Outline each Trypanosoma brucei.
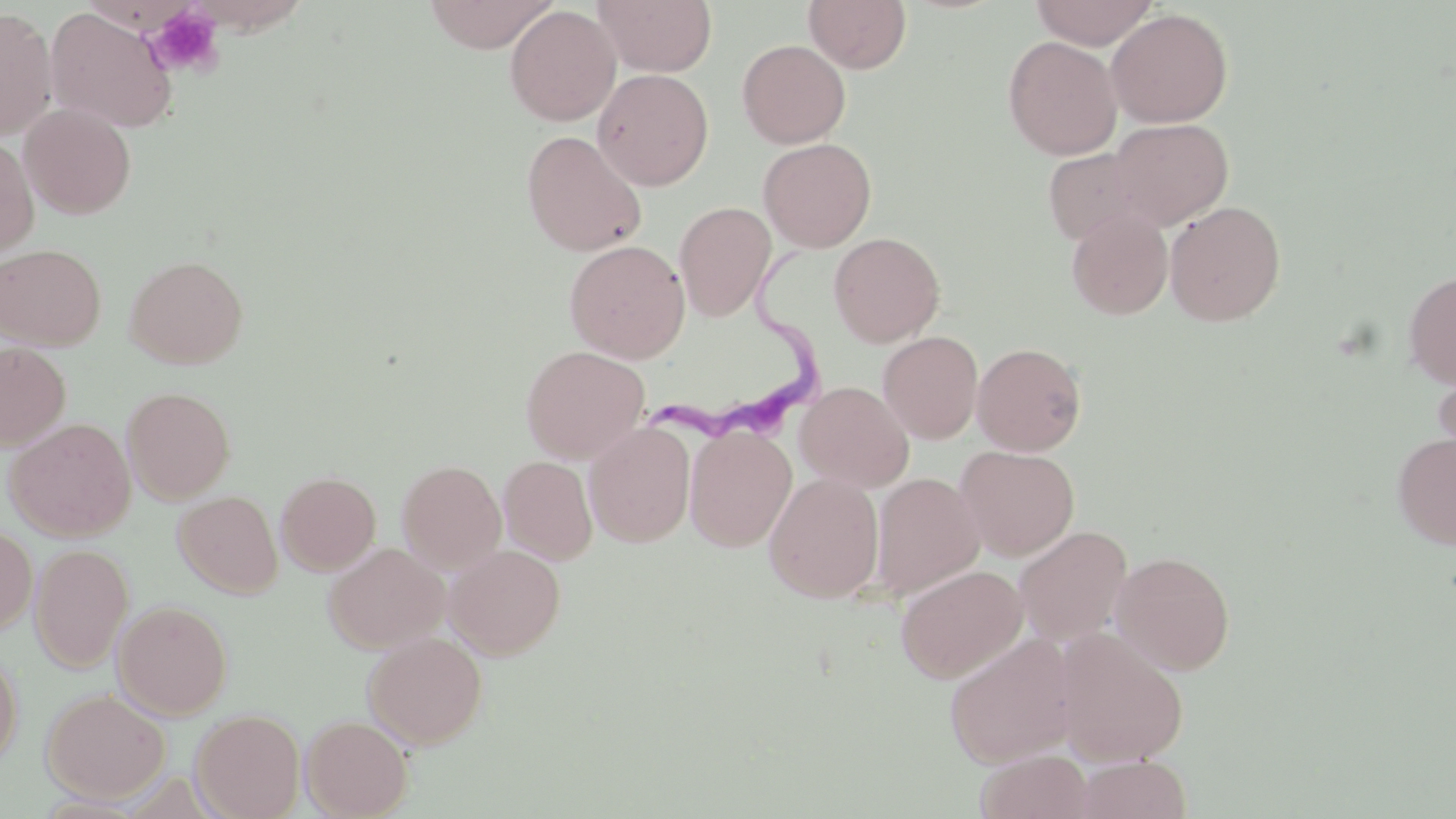
Approximate bounding boxes as [x1, y1, x2, y2] in pixels.
Trypanosoma brucei: [637, 251, 818, 446].

Summary:
  - Platelet locations: [147, 5, 225, 78]
  - Uninfected red blood cell locations: [421, 0, 558, 53], [594, 0, 717, 76], [804, 0, 912, 73], [1029, 0, 1160, 49], [504, 5, 621, 126], [0, 7, 58, 141], [45, 7, 178, 134], [1105, 8, 1233, 127], [1002, 35, 1122, 160], [737, 39, 850, 148], [592, 68, 714, 190], [20, 103, 136, 219], [1109, 117, 1234, 229], [521, 130, 647, 256], [0, 134, 39, 259], [758, 137, 877, 252], [1042, 148, 1150, 246], [1165, 200, 1286, 326], [674, 202, 776, 322], [1066, 207, 1173, 320], [828, 232, 945, 347], [564, 239, 690, 363], [0, 243, 106, 350], [125, 254, 248, 369], [1402, 270, 1456, 388], [878, 331, 983, 443], [0, 342, 71, 451], [972, 342, 1087, 455], [521, 345, 650, 464], [1432, 360, 1456, 478], [794, 381, 915, 493], [122, 386, 236, 504], [4, 417, 137, 541], [585, 421, 696, 547], [684, 425, 797, 552], [1392, 431, 1456, 550], [956, 445, 1080, 560], [498, 455, 597, 565], [397, 459, 507, 572], [275, 471, 381, 575], [764, 472, 885, 603], [872, 472, 985, 601], [172, 490, 283, 598], [0, 525, 37, 636], [1013, 525, 1133, 646], [323, 542, 449, 653], [30, 543, 133, 673], [445, 544, 566, 660], [1110, 551, 1235, 674], [895, 563, 1028, 683], [113, 600, 232, 720], [1053, 628, 1189, 766], [363, 630, 488, 749], [944, 631, 1078, 768], [0, 648, 23, 768], [41, 688, 170, 802], [191, 709, 305, 819], [300, 714, 413, 818], [976, 749, 1095, 819], [1074, 755, 1191, 818]
  - Slide-level diagnosis: Trypanosoma brucei
  - Modality: optical microscopy
  - Stain: May-Grünwald-Giemsa
  - Field of view: single
  - Preparation: thin blood film
  - Magnification: 1000x
  - Image size: 1456×819 pixels